Classify this cell by malaria status.
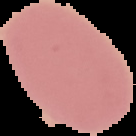

It is uninfected.

From a thin blood smear. Image is 136×136 pixels. Segmented cell region on a black background.